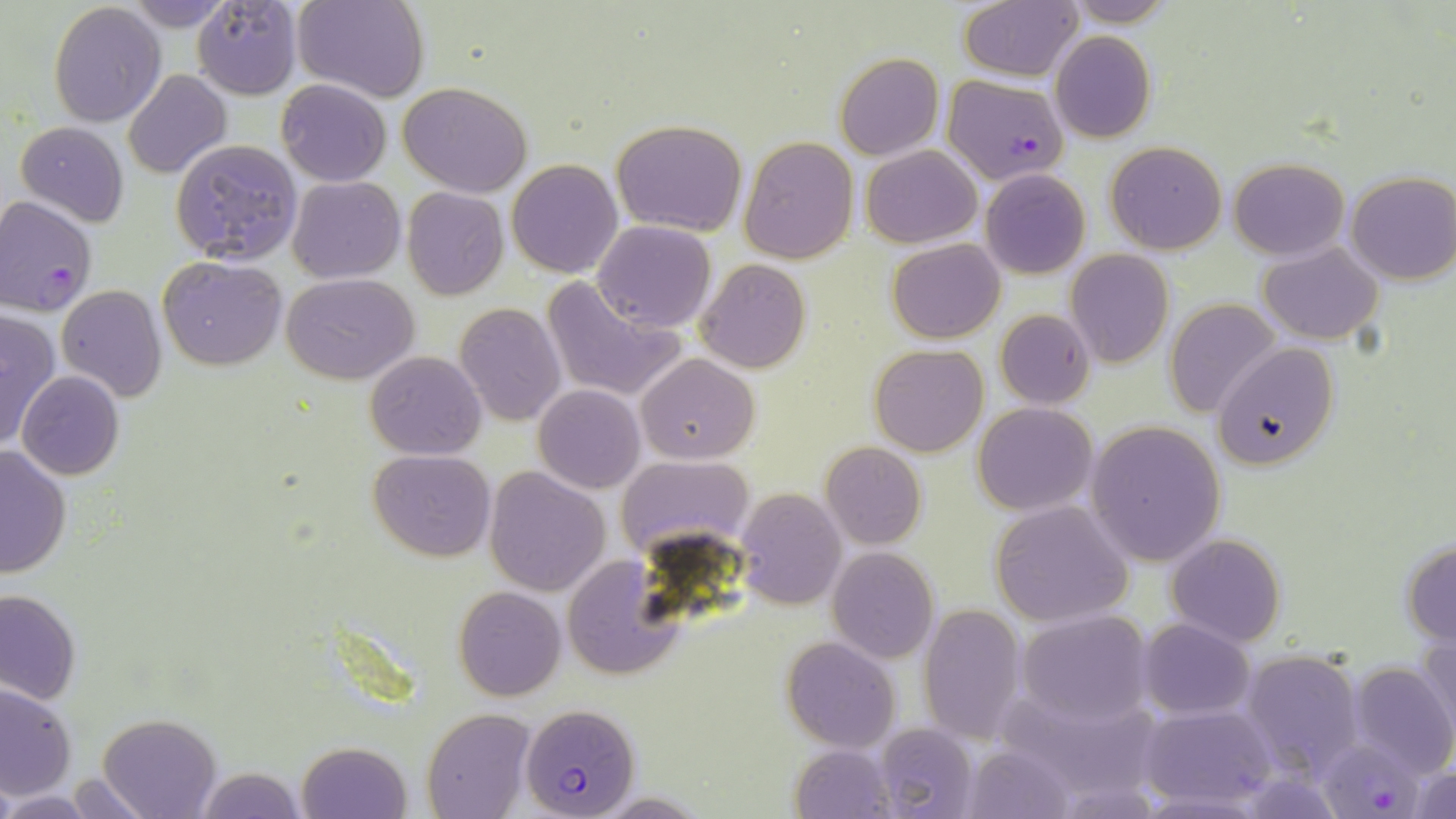
slide_level_diagnosis: Plasmodium falciparum
uninfected_red_blood_cell_locations: 'approximate bounding boxes as (x1,y1)-(x2,y2) corner pairs in pixels: (120,0)-(242,30), (192,0)-(303,100), (293,0)-(428,102), (957,0)-(1083,83), (1055,0)-(1183,27), (48,3)-(166,127), (1050,30)-(1156,143), (834,54)-(943,160), (122,70)-(232,180), (276,79)-(391,186), (397,81)-(533,199), (609,118)-(748,237), (16,120)-(130,226), (739,136)-(857,263), (172,138)-(303,266), (1105,141)-(1227,254), (861,145)-(982,249), (507,158)-(624,278), (1227,158)-(1349,260), (980,170)-(1090,279), (1345,171)-(1456,285), (287,175)-(405,283), (401,187)-(509,301), (592,221)-(715,332), (887,240)-(1004,343), (1258,242)-(1385,345), (1065,249)-(1173,368), (159,256)-(288,371), (696,259)-(811,373), (283,274)-(418,385), (540,274)-(687,404), (57,284)-(168,403), (1165,299)-(1283,419), (454,301)-(567,427), (0,307)-(63,454), (993,309)-(1095,410), (1212,344)-(1338,469), (869,345)-(990,458), (365,351)-(486,459), (636,354)-(760,464), (16,370)-(124,480), (534,385)-(645,494), (972,402)-(1097,516), (1083,420)-(1227,567), (820,442)-(927,551), (0,443)-(73,578), (368,449)-(497,562), (615,454)-(754,565), (484,466)-(610,596), (735,488)-(848,610), (988,501)-(1133,627), (1166,534)-(1286,646), (1401,540)-(1456,646), (827,548)-(938,663), (563,556)-(683,679), (453,586)-(566,701), (0,589)-(82,704), (918,604)-(1027,745), (1016,612)-(1152,729), (1137,620)-(1256,719), (1419,635)-(1456,747), (782,636)-(900,753), (1240,649)-(1364,778), (1346,660)-(1456,778), (0,682)-(76,800), (999,690)-(1163,803), (1137,704)-(1279,811), (423,709)-(532,819), (97,714)-(220,819), (871,723)-(980,819), (297,740)-(412,818), (789,742)-(897,818), (959,744)-(1079,819), (1409,761)-(1456,817), (194,766)-(306,819), (64,775)-(157,818), (1,791)-(103,817)'
modality: optical microscopy
field_of_view: one of a larger specimen
magnification: 1000x
plasmodium_falciparum_infected_red_blood_cell_locations: 'approximate bounding boxes as (x1,y1)-(x2,y2) corner pairs in pixels: (944,75)-(1068,184), (0,194)-(99,316), (521,702)-(641,818), (1321,742)-(1420,819)'
image_size: 1456×819 pixels
preparation: thin blood smear
stain: May-Grünwald-Giemsa